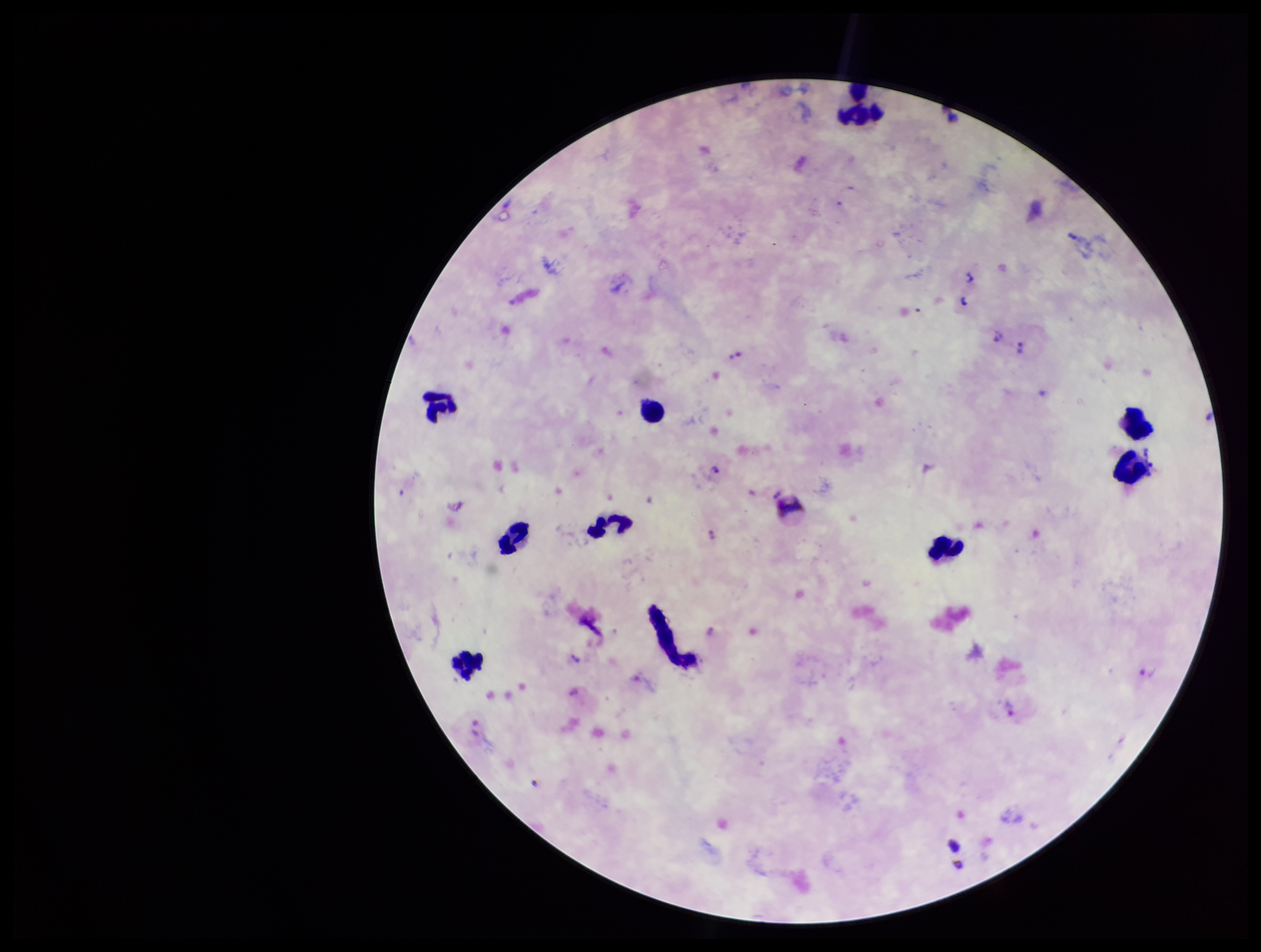 Smartphone photograph taken through the eyepiece of a microscope. Single field of view. Patient malaria status: infected. Preparation: thick blood smear. Plasmodium parasites: identified. Parasite count: 10. Image is 1261×952 pixels. Leukocyte count: 9. Species reported for this patient: Plasmodium vivax. Stained with Giemsa.